Assess for Plasmodium parasites.
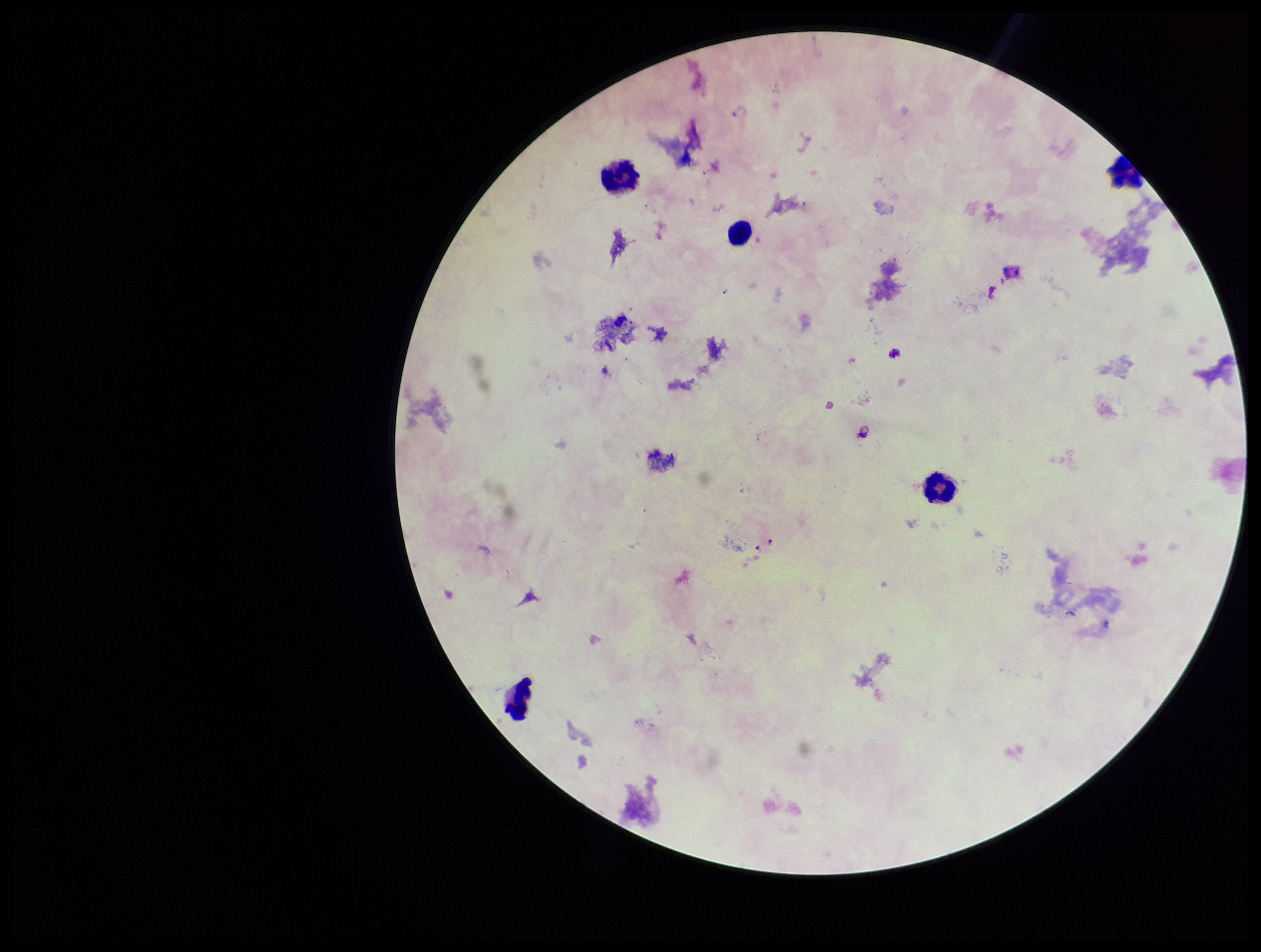
None detected.

Summary:
  - Leukocyte count: 5
  - Image size: 1261×952 pixels
  - Stain: Giemsa
  - Parasite count: 0
  - Patient malaria status: infected
  - Species reported for this patient: Plasmodium falciparum
  - Field of view: one from this slide
  - Capture: smartphone photograph through the microscope eyepiece
  - Preparation: thick